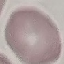

Result: no malaria parasites seen. Automatically extracted cell patch, resized to 64 × 64 pixels. Photographed with a smartphone camera at the microscope eyepiece. Thin blood smear. Giemsa-stained preparation.